Report the malaria status of this cell.
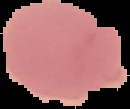

It is uninfected.

Summary:
  - Image type: segmented cell region with the area outside set to black
  - Preparation: thin blood smear
  - Image size: 130×109 pixels